Describe the morphology of the red blood cells.
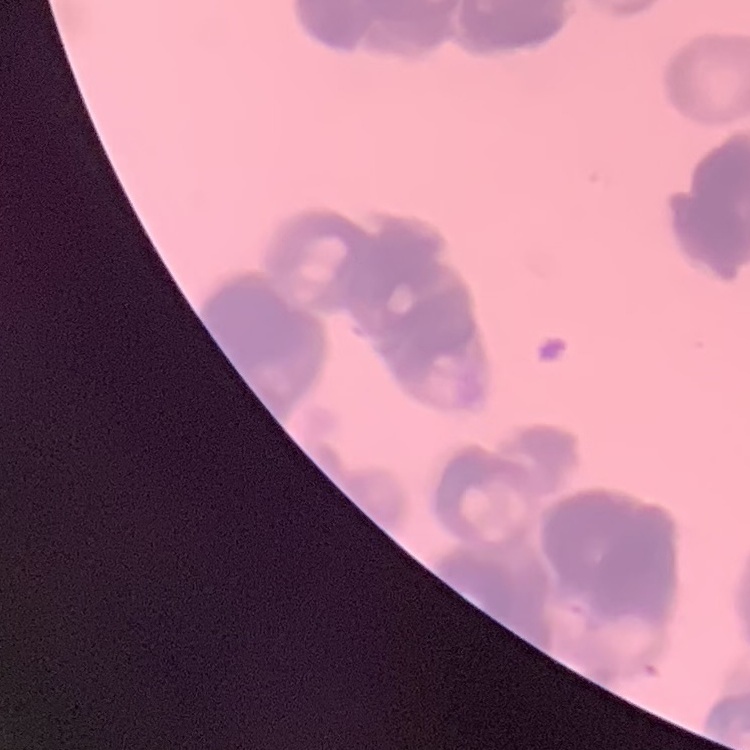
They show rouleaux formation.

Summary:
  - Preparation: thin blood film
  - Image type: one tile cut from a larger photomicrograph
  - Stain: Field's or Giemsa